Report the malaria status of this cell.
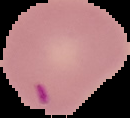
Parasitized.

Summary:
  - Image type: segmented cell region with the area outside set to black
  - Preparation: thin blood smear
  - Image size: 130×118 pixels